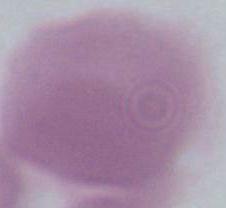
identification = red blood cell
magnification = 1000x
modality = photomicrograph